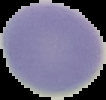

Result: negative for Plasmodium parasites. Segmented cell region on a black background. From a thin blood smear. Image is 106×100 pixels.